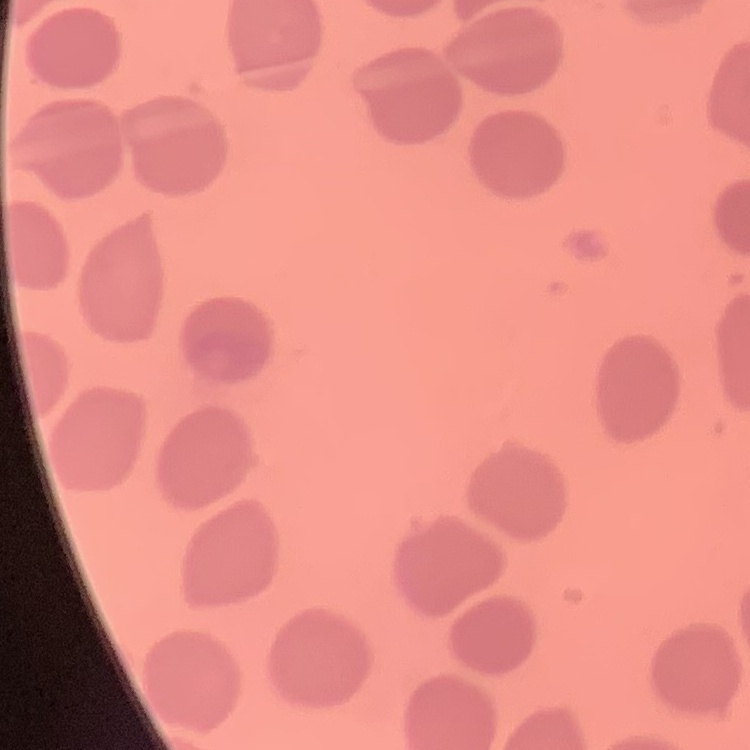
Summary:
  - Erythrocyte morphology: no rouleaux formation
  - Preparation: thin blood smear
  - Image type: one tile cut from a larger photomicrograph
  - Stain: Field's or Giemsa